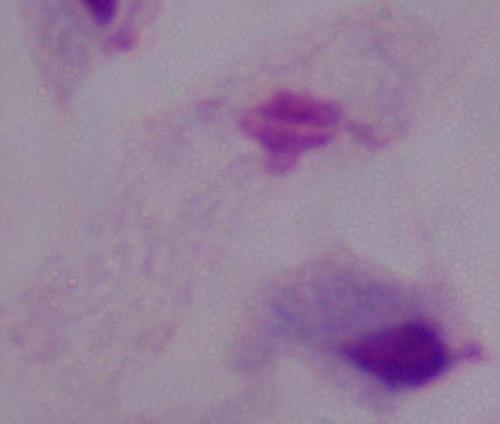 A trichomonad is shown. Captured at 1000x magnification. Photomicrograph.